State which parasite is depicted.
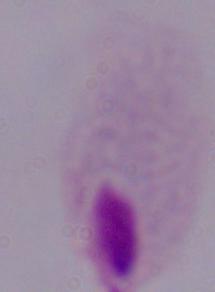

A trichomonad.

Photomicrograph. 1000x magnification.